Assess this cell for malaria.
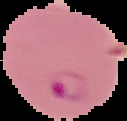
It is parasitized.

Summary:
  - Image type: segmented cell region on a black background
  - Preparation: thin blood smear
  - Image size: 127×121 pixels